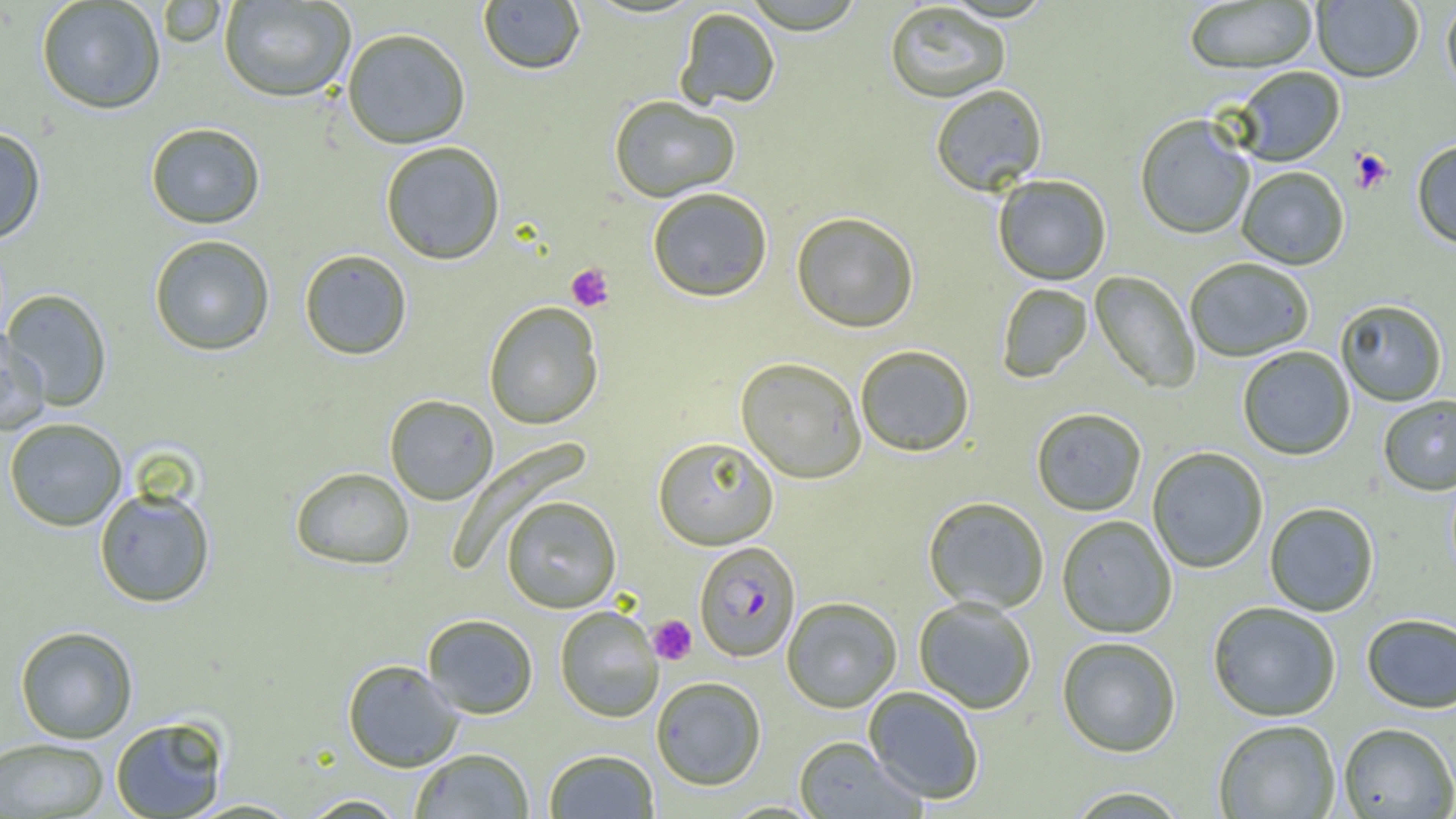
Approximate bounding boxes as (x1, y1, x2, y2) in pixels. Uninfected red blood cell locations: (36, 0, 166, 115), (218, 0, 356, 103), (741, 0, 867, 34), (1312, 0, 1424, 84), (157, 1, 227, 48), (477, 1, 585, 75), (1184, 1, 1318, 75), (1441, 1, 1456, 100), (884, 2, 1011, 103), (674, 6, 781, 110), (341, 28, 471, 149), (1234, 67, 1345, 166), (930, 85, 1047, 197), (608, 95, 740, 203), (1135, 115, 1255, 241), (145, 122, 266, 229), (0, 126, 47, 245), (379, 141, 505, 265), (1412, 141, 1456, 251), (1237, 167, 1349, 271), (993, 175, 1112, 286), (647, 188, 773, 303), (791, 212, 919, 334), (148, 235, 276, 356), (299, 248, 413, 360), (1185, 258, 1315, 362), (1090, 270, 1200, 394), (996, 283, 1093, 383), (2, 289, 113, 411), (1336, 300, 1447, 407), (483, 302, 604, 430), (0, 328, 49, 435), (855, 345, 974, 457), (1238, 346, 1355, 460), (735, 357, 867, 483), (384, 394, 498, 505), (1378, 395, 1456, 495), (1031, 407, 1147, 516), (3, 417, 128, 531), (653, 436, 779, 549), (1147, 447, 1268, 574), (290, 466, 414, 570), (94, 486, 215, 608), (501, 495, 621, 613), (923, 496, 1050, 613), (1264, 502, 1379, 617), (1056, 515, 1177, 638), (782, 597, 902, 712), (913, 597, 1037, 714), (1208, 602, 1341, 722), (555, 605, 663, 722), (422, 613, 538, 719), (1361, 614, 1456, 714), (14, 626, 138, 743), (1057, 637, 1181, 758), (342, 659, 464, 772), (651, 676, 767, 790), (863, 686, 984, 805), (110, 715, 230, 818), (1214, 720, 1341, 819), (1338, 724, 1456, 818), (793, 736, 923, 818), (0, 737, 110, 818), (410, 748, 534, 818), (544, 749, 660, 818), (1064, 786, 1192, 818), (297, 794, 409, 818), (181, 798, 305, 818). Platelet locations: (1350, 150, 1393, 194), (566, 263, 614, 312), (648, 615, 697, 665). Plasmodium falciparum-infected red blood cell locations: (694, 541, 801, 662). Slide-level diagnosis: Plasmodium falciparum. Thin blood film. Image is 1456×819 pixels. One field of a larger specimen. 1000x magnification. Optical microscopy.